State which parasite is depicted.
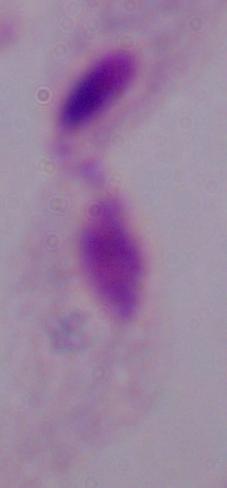
This is a trichomonad.

modality = micrograph
magnification = 1000x